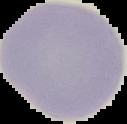
Summary:
  - Malaria status: uninfected
  - Image type: segmented cell region on a black background
  - Image size: 127×124 pixels
  - Preparation: thin blood film